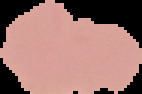

malaria status = uninfected
image type = cell region segmented out of the field of view; surrounding area masked to black
preparation = thin blood film
image size = 142×94 pixels